Classify this cell by malaria status.
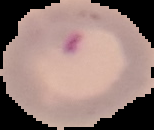
It is parasitized.

Summary:
  - Preparation: thin blood film
  - Image size: 154×130 pixels
  - Image type: segmented cell region on a black background